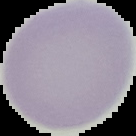 From a thin blood film. The area outside the segmented cell region is set to black. Malaria status: uninfected. Image is 136×136 pixels.